Assess this cell for malaria.
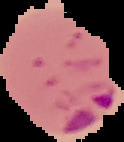
Parasitized.

Image is 124×142 pixels. The area outside the segmented cell region is set to black. From a thin blood film.